Classify this cell by malaria status.
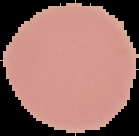
Uninfected.

Image is 139×136 pixels. From a thin blood film. The area outside the segmented cell region is set to black.